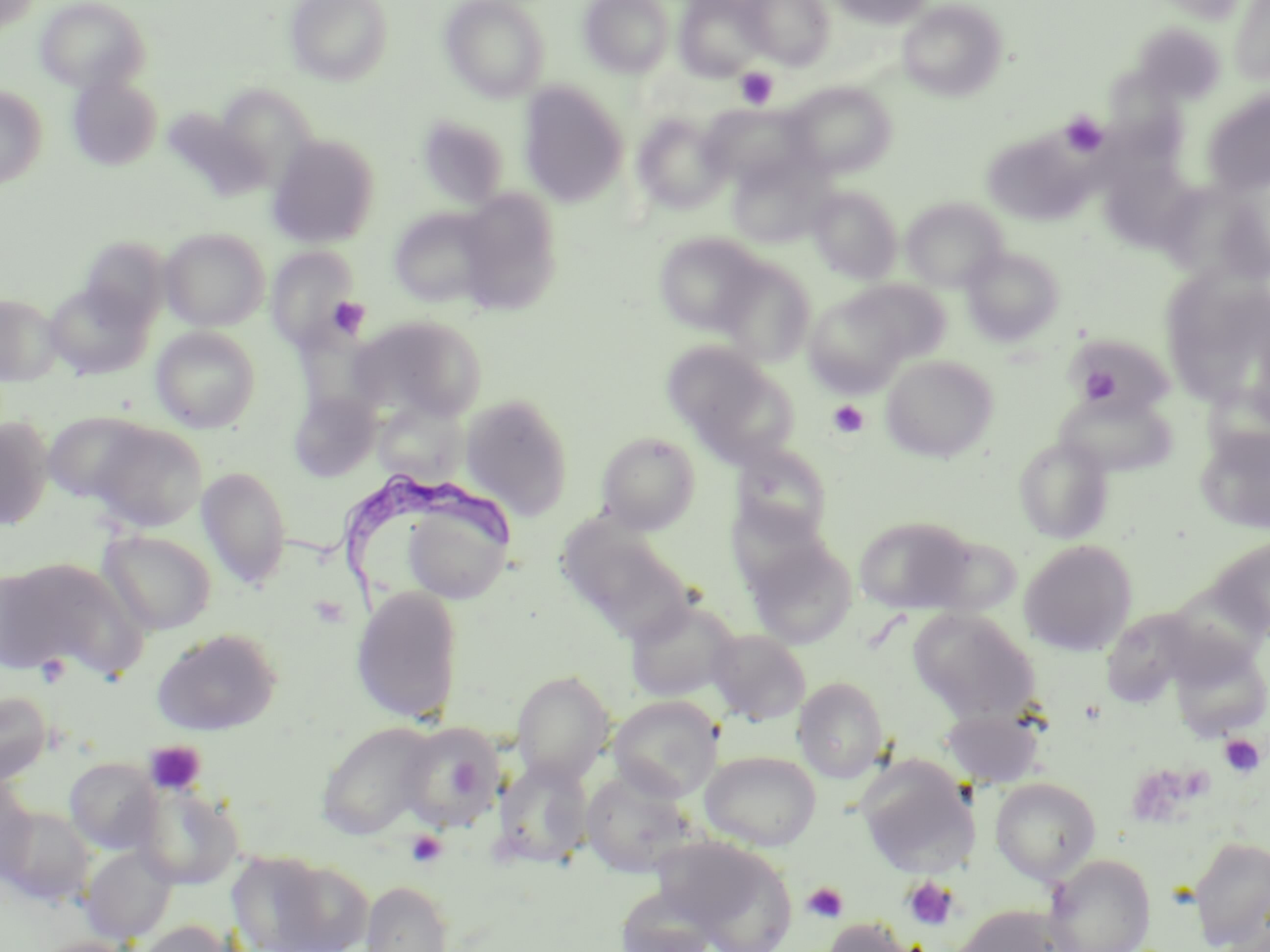
slide-level diagnosis = Trypanosoma brucei
preparation = thin blood smear
stain = May-Grünwald-Giemsa
Trypanosoma brucei locations = approximate bounding boxes as (x1,y1)-(x2,y2) corner pairs in pixels: (286,471)-(526,620)
modality = optical microscopy
image size = 1270×952 pixels
field of view = one of a larger specimen
magnification = 1000x
platelet locations = approximate bounding boxes as (x1,y1)-(x2,y2) corner pairs in pixels: (735,68)-(778,108), (1059,112)-(1109,158), (331,296)-(372,336), (1079,364)-(1125,404), (827,401)-(870,439), (35,653)-(72,689), (1219,734)-(1264,777), (143,740)-(207,797), (1125,765)-(1196,828), (1176,765)-(1215,802), (405,830)-(448,869), (902,876)-(961,931), (802,882)-(849,923)
uninfected red blood cell locations = approximate bounding boxes as (x1,y1)-(x2,y2) corner pairs in pixels: (0,0)-(42,36), (36,0)-(150,93), (285,0)-(393,85), (441,0)-(550,102), (579,0)-(674,77), (675,0)-(768,81), (741,0)-(835,69), (829,0)-(932,28), (1152,0)-(1251,24), (897,1)-(1007,101), (1229,1)-(1270,84), (1133,21)-(1226,105), (67,73)-(163,171), (1107,73)-(1195,168), (519,82)-(629,207), (784,82)-(896,178), (216,83)-(317,184), (0,85)-(47,188), (1201,90)-(1270,196), (698,103)-(811,190), (632,112)-(731,214), (416,114)-(511,209), (981,132)-(1087,226), (267,133)-(381,248), (727,153)-(831,248), (1111,160)-(1199,250), (1164,184)-(1270,289), (808,185)-(903,283), (455,189)-(562,314), (900,197)-(1008,292), (389,207)-(498,308), (160,227)-(269,331), (654,231)-(764,335), (79,237)-(170,330), (266,245)-(362,352), (961,246)-(1065,345), (715,257)-(815,366), (1166,278)-(1258,409), (843,279)-(950,366), (44,281)-(153,379), (803,289)-(915,394), (0,294)-(64,385), (357,315)-(487,419), (151,326)-(260,432), (1064,334)-(1176,417), (665,344)-(796,464), (880,355)-(998,462), (289,389)-(380,482), (1054,390)-(1179,477), (460,393)-(573,518), (380,404)-(471,485), (44,411)-(152,505), (0,417)-(53,530), (87,420)-(208,532), (1195,426)-(1270,534), (597,432)-(700,533), (1014,437)-(1114,544), (732,445)-(833,546), (197,466)-(293,589), (398,499)-(513,605), (726,499)-(832,595), (854,515)-(977,614), (562,524)-(695,643), (99,529)-(217,635), (1209,536)-(1270,641), (745,538)-(858,649), (1018,539)-(1138,656), (0,557)-(143,681), (1,565)-(71,672), (350,584)-(465,724), (1156,584)-(1261,686), (624,596)-(740,703), (1105,604)-(1194,709), (909,608)-(1041,723), (151,628)-(283,736), (706,629)-(811,725), (1168,641)-(1270,741), (511,670)-(615,785), (793,676)-(889,782), (0,690)-(53,785), (608,695)-(724,801), (941,705)-(1046,789), (315,720)-(438,840), (397,722)-(503,833), (699,750)-(822,851), (856,756)-(975,876), (64,757)-(160,854), (494,759)-(595,868), (579,769)-(701,880), (990,776)-(1101,884), (0,777)-(38,882), (134,783)-(244,890), (2,806)-(94,904), (1188,835)-(1270,951), (657,836)-(798,951), (80,845)-(177,944), (229,851)-(364,951), (1044,854)-(1156,952), (360,880)-(453,952), (613,885)-(721,952), (951,904)-(1076,952), (820,918)-(918,952), (130,919)-(239,952), (28,936)-(141,952)